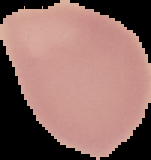

Summary:
  - Image size: 151×160 pixels
  - Preparation: thin blood film
  - Image type: segmented cell region with the area outside set to black
  - Result: no malaria parasites detected